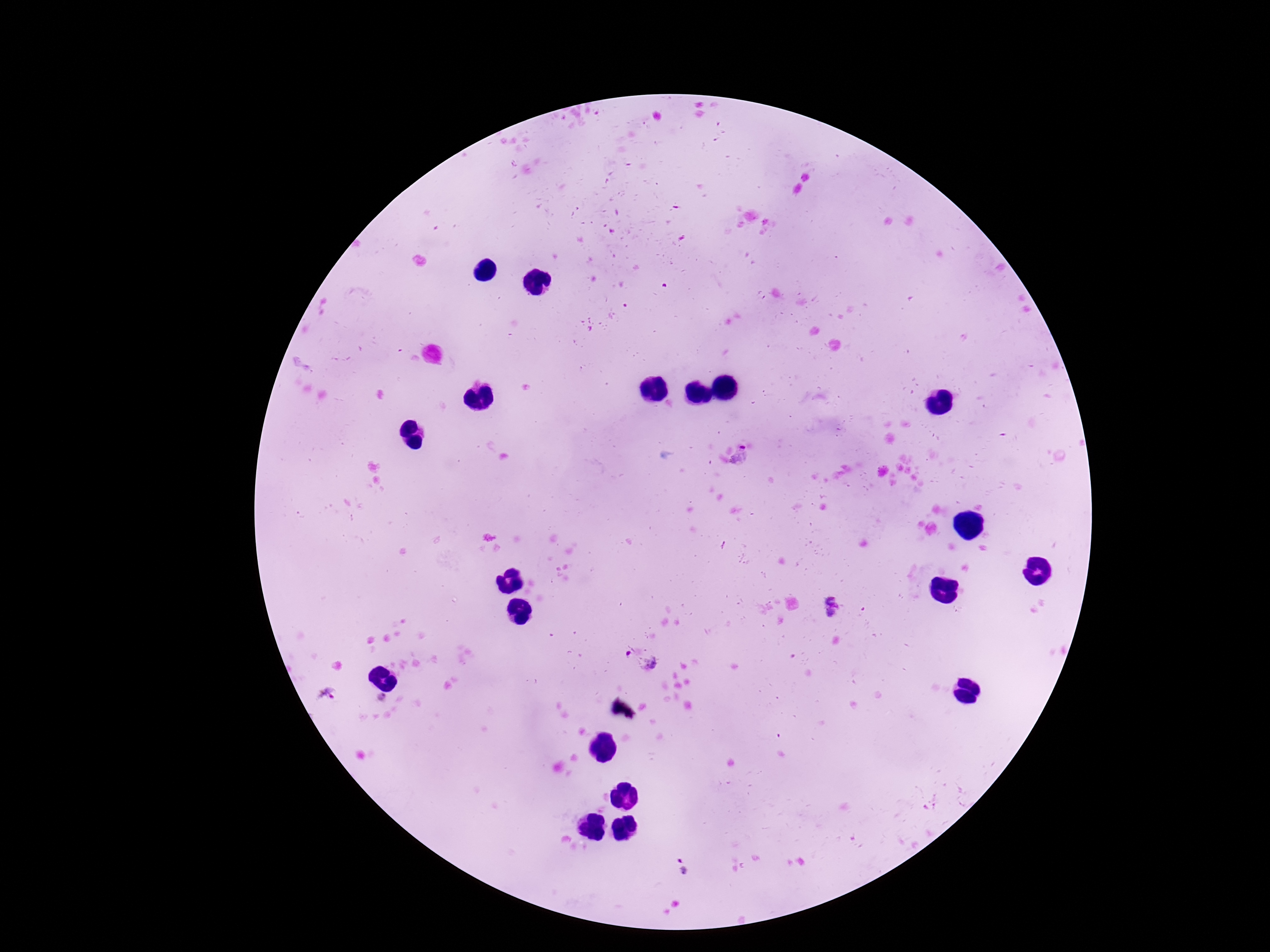

Approximate object centers, in pixels from the top-left corner.
Summary:
  - Plasmodium parasite locations: (x=742, y=458), (x=830, y=607), (x=641, y=662), (x=328, y=696), (x=681, y=867)
  - Image size: 1270×952 pixels
  - Capture: smartphone camera through the microscope eyepiece
  - Field of view: one from this slide
  - Stain: Giemsa
  - Magnification: 100x
  - Preparation: thick blood film
  - Patient malaria status: infected